Locate every blood parasite and identify its species.
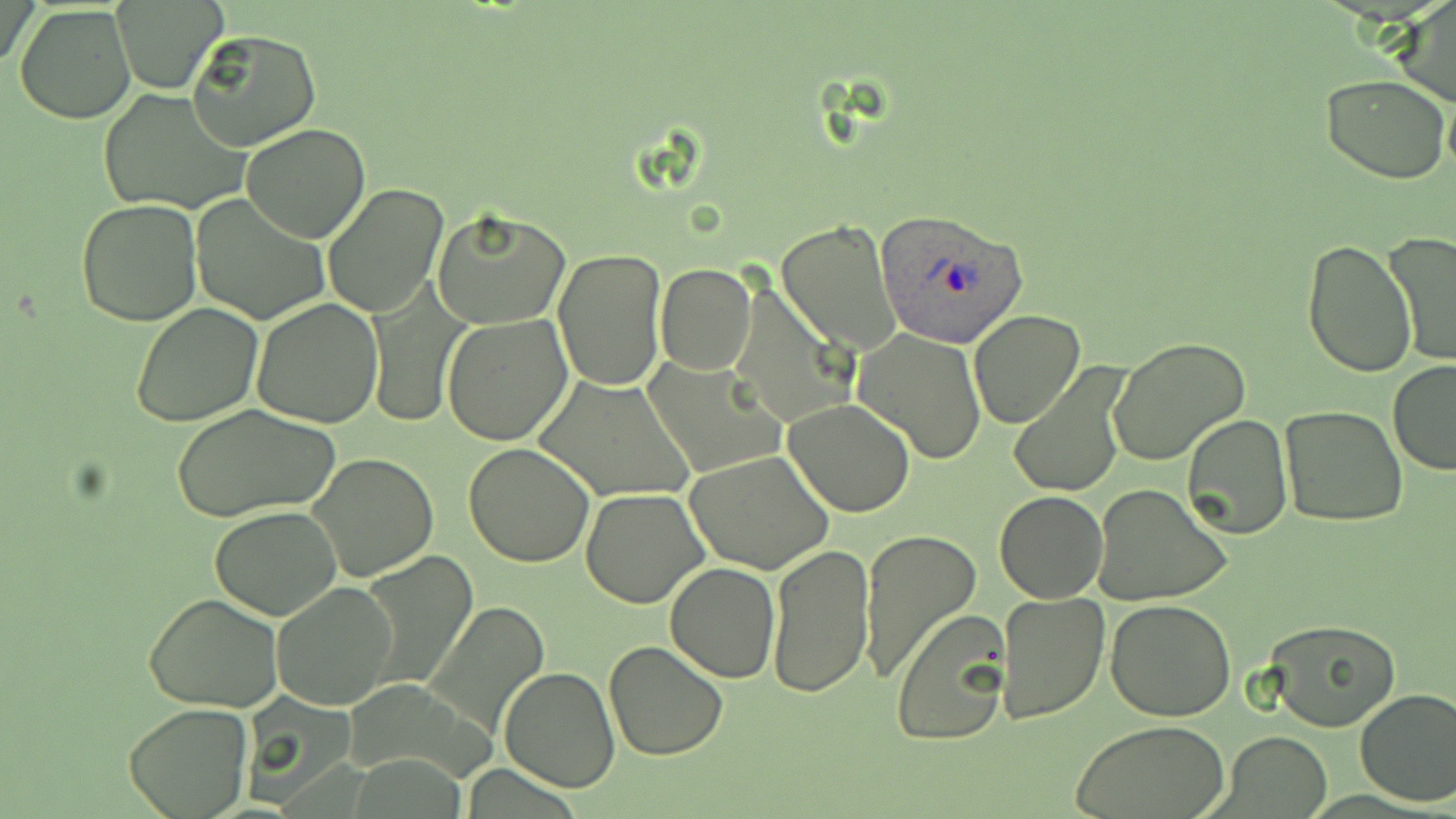
Approximate bounding boxes as [x1, y1, x2, y2] in pixels.
Plasmodium ovale-infected red blood cells: [878, 210, 1025, 349].
No Plasmodium falciparum, Plasmodium malariae, Plasmodium vivax, Babesia divergens, or Trypanosoma brucei observed.

Summary:
  - Uninfected red blood cell locations: [3, 0, 39, 75], [1393, 0, 1456, 108], [112, 2, 226, 92], [14, 4, 137, 124], [187, 28, 320, 152], [146, 68, 308, 198], [1321, 75, 1452, 185], [98, 88, 248, 214], [1443, 90, 1456, 180], [242, 123, 369, 244], [322, 183, 451, 320], [190, 193, 332, 327], [75, 197, 203, 326], [432, 208, 570, 329], [778, 217, 901, 358], [1384, 230, 1456, 367], [1304, 238, 1415, 376], [552, 247, 667, 392], [656, 263, 756, 375], [729, 281, 853, 428], [365, 288, 468, 425], [251, 299, 385, 428], [131, 303, 262, 427], [969, 309, 1086, 429], [441, 315, 571, 447], [854, 330, 988, 465], [1109, 337, 1251, 467], [645, 358, 787, 481], [1387, 361, 1456, 475], [1008, 363, 1130, 497], [534, 375, 694, 502], [783, 400, 916, 517], [170, 403, 343, 523], [1278, 406, 1407, 528], [1182, 413, 1292, 540], [465, 442, 596, 567], [684, 449, 836, 575], [306, 450, 441, 583], [1092, 484, 1233, 607], [580, 488, 711, 608], [994, 490, 1108, 603], [210, 506, 342, 620], [859, 528, 981, 682], [767, 542, 875, 699], [363, 552, 479, 690], [664, 561, 780, 683], [271, 579, 398, 709], [994, 589, 1110, 725], [143, 594, 283, 712], [1106, 599, 1237, 721], [428, 603, 548, 737], [890, 608, 1012, 747], [1263, 619, 1400, 732], [604, 640, 728, 761], [499, 666, 619, 793], [1354, 688, 1456, 807], [123, 703, 254, 818], [1074, 719, 1229, 818], [1220, 730, 1331, 817]
  - Slide-level diagnosis: Plasmodium ovale
  - Preparation: thin blood smear
  - Field of view: one of a larger specimen
  - Stain: May-Grünwald-Giemsa
  - Image size: 1456×819 pixels
  - Modality: optical microscopy
  - Magnification: 1000x